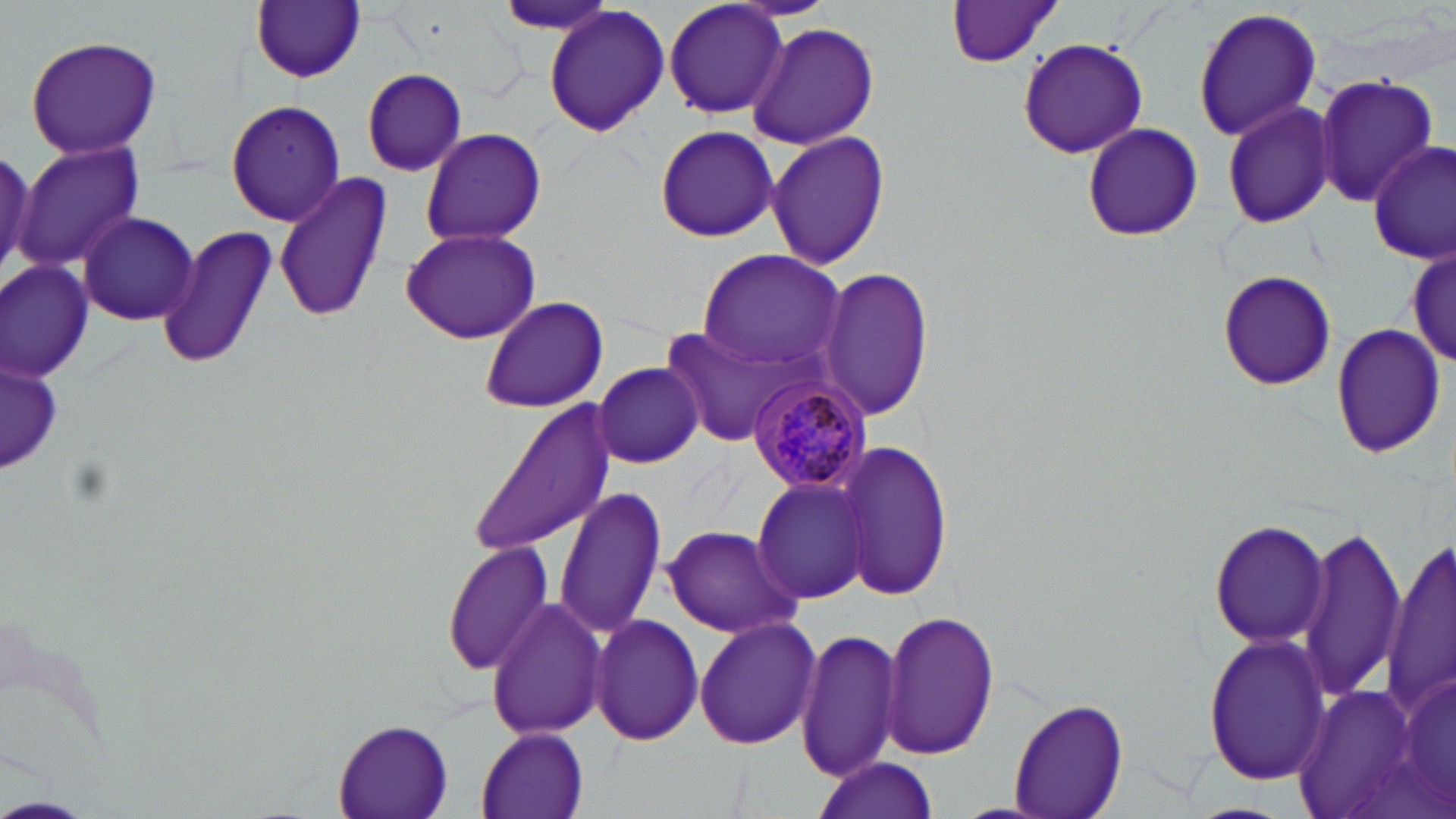

slide-level diagnosis = Plasmodium malariae
uninfected red blood cell locations = approximate bounding boxes as (x1, y1, x2, y2) in pixels: (660, 0, 790, 120), (252, 1, 366, 84), (491, 1, 624, 38), (945, 2, 1067, 69), (542, 4, 669, 140), (1193, 5, 1321, 141), (746, 20, 880, 151), (24, 34, 163, 159), (1017, 37, 1148, 162), (360, 67, 468, 176), (1313, 74, 1438, 210), (226, 98, 345, 227), (1220, 98, 1338, 231), (1080, 122, 1203, 242), (653, 123, 778, 242), (420, 128, 547, 247), (766, 129, 889, 272), (15, 141, 147, 273), (1370, 141, 1454, 265), (45, 168, 177, 312), (273, 170, 394, 327), (75, 212, 200, 327), (157, 225, 280, 371), (399, 226, 542, 345), (1406, 246, 1456, 367), (698, 248, 846, 372), (0, 262, 93, 382), (819, 265, 932, 421), (1216, 271, 1338, 392), (477, 294, 610, 414), (1329, 321, 1449, 460), (667, 325, 810, 445), (4, 356, 62, 473), (594, 362, 702, 468), (470, 404, 616, 557), (837, 440, 953, 602), (753, 476, 875, 604), (554, 486, 667, 638), (1209, 519, 1330, 648), (661, 525, 801, 637), (1295, 529, 1407, 699), (1385, 537, 1455, 712), (442, 539, 556, 676), (486, 597, 608, 741), (880, 607, 1000, 761), (589, 612, 703, 747), (694, 615, 822, 751), (800, 626, 904, 783), (1202, 630, 1331, 788), (1395, 669, 1456, 810), (1293, 680, 1422, 819), (1008, 697, 1129, 819), (333, 720, 455, 819), (476, 726, 591, 819), (812, 759, 939, 819)
Plasmodium malariae-infected red blood cell locations = approximate bounding boxes as (x1, y1, x2, y2) in pixels: (744, 374, 875, 495)
stain = May-Grünwald-Giemsa
image size = 1456×819 pixels
modality = light microscopy
magnification = 1000x
preparation = thin blood film
field of view = one of a larger specimen